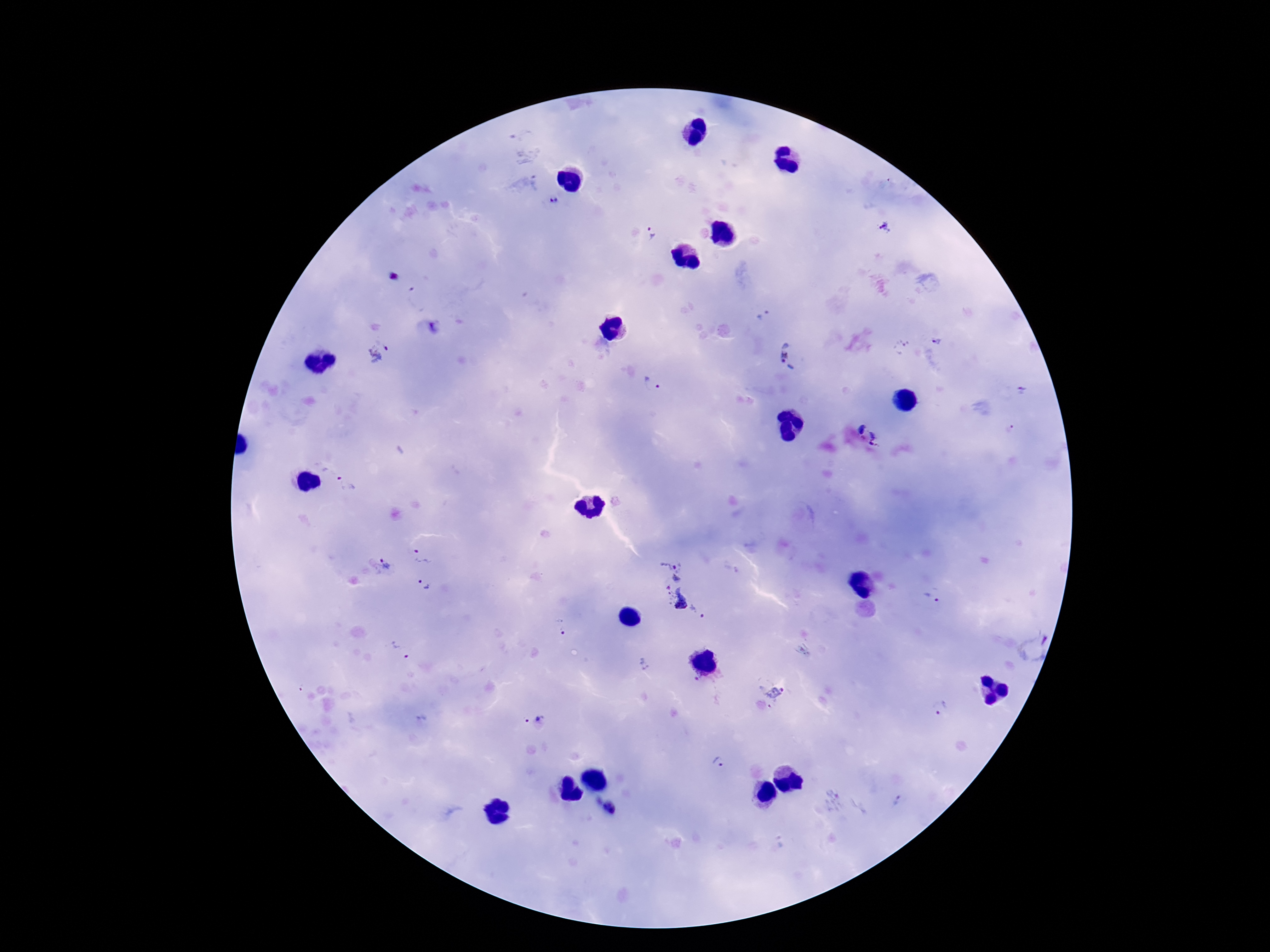

Approximate object centers, in pixels from the top-left corner.
Summary:
  - Plasmodium parasite locations: (x=554, y=201), (x=885, y=228), (x=652, y=233), (x=395, y=277), (x=761, y=315), (x=937, y=340), (x=902, y=345), (x=378, y=351), (x=791, y=356), (x=654, y=384), (x=1023, y=391), (x=1010, y=428), (x=869, y=433), (x=346, y=484), (x=422, y=557), (x=384, y=567), (x=673, y=568), (x=423, y=585), (x=931, y=597), (x=683, y=603), (x=560, y=627), (x=1032, y=646), (x=402, y=649), (x=644, y=664), (x=698, y=681), (x=769, y=692), (x=940, y=707), (x=533, y=716), (x=719, y=764), (x=898, y=801), (x=608, y=808)
  - Capture: smartphone camera through the microscope eyepiece
  - Stain: Giemsa
  - Preparation: thick peripheral-blood smear
  - Magnification: 100x
  - Patient malaria status: positive
  - Image size: 1270×952 pixels
  - Field of view: single